Name the blood parasite species.
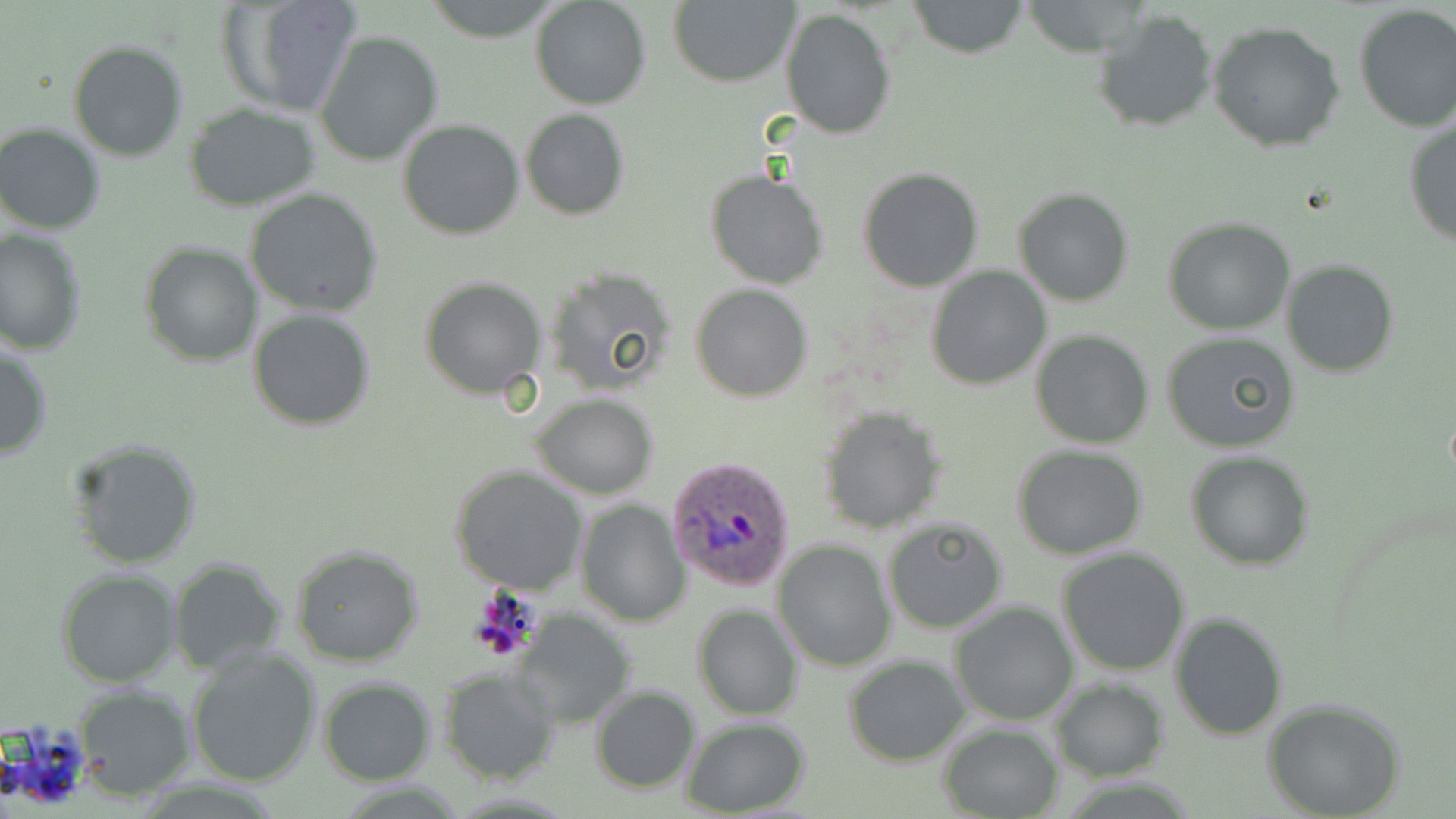
Plasmodium ovale.

Approximate bounding boxes as [x1, y1, x2, y2] in pixels. Uninfected red blood cell locations: [218, 0, 364, 120], [531, 0, 651, 110], [670, 0, 799, 87], [420, 1, 564, 40], [905, 1, 1031, 58], [1351, 4, 1456, 132], [1091, 6, 1219, 134], [781, 8, 897, 141], [1207, 20, 1349, 153], [315, 30, 444, 167], [67, 39, 189, 162], [182, 105, 323, 210], [519, 108, 630, 219], [1403, 117, 1456, 248], [397, 118, 525, 241], [1, 123, 105, 235], [857, 168, 985, 292], [706, 171, 829, 291], [1013, 187, 1135, 307], [246, 189, 384, 317], [1163, 214, 1296, 334], [1, 228, 87, 354], [140, 241, 264, 366], [1280, 259, 1399, 379], [926, 267, 1051, 389], [543, 269, 677, 395], [420, 277, 547, 400], [691, 283, 813, 402], [247, 309, 375, 431], [1030, 329, 1155, 449], [1160, 331, 1301, 455], [0, 338, 53, 461], [530, 393, 659, 498], [818, 406, 946, 532], [67, 439, 204, 571], [1012, 444, 1149, 561], [1186, 450, 1313, 569], [449, 465, 588, 596], [575, 498, 690, 626], [881, 518, 1009, 634], [772, 540, 894, 671], [289, 542, 424, 667], [1056, 548, 1191, 678], [168, 558, 287, 674], [57, 569, 182, 687], [948, 600, 1079, 726], [691, 604, 803, 721], [514, 611, 636, 728], [1169, 612, 1288, 741], [186, 647, 323, 788], [844, 655, 969, 767], [439, 667, 560, 785], [319, 676, 435, 785], [1050, 678, 1170, 780], [71, 685, 195, 798], [591, 685, 701, 795], [1261, 697, 1407, 819], [682, 717, 811, 817], [940, 722, 1062, 819]. Plasmodium ovale-infected red blood cell locations: [670, 458, 798, 592]. Optical microscopy. 1000x magnification. One field of a larger specimen. May-Grünwald-Giemsa-stained preparation. Image is 1456×819 pixels. Thin blood film.